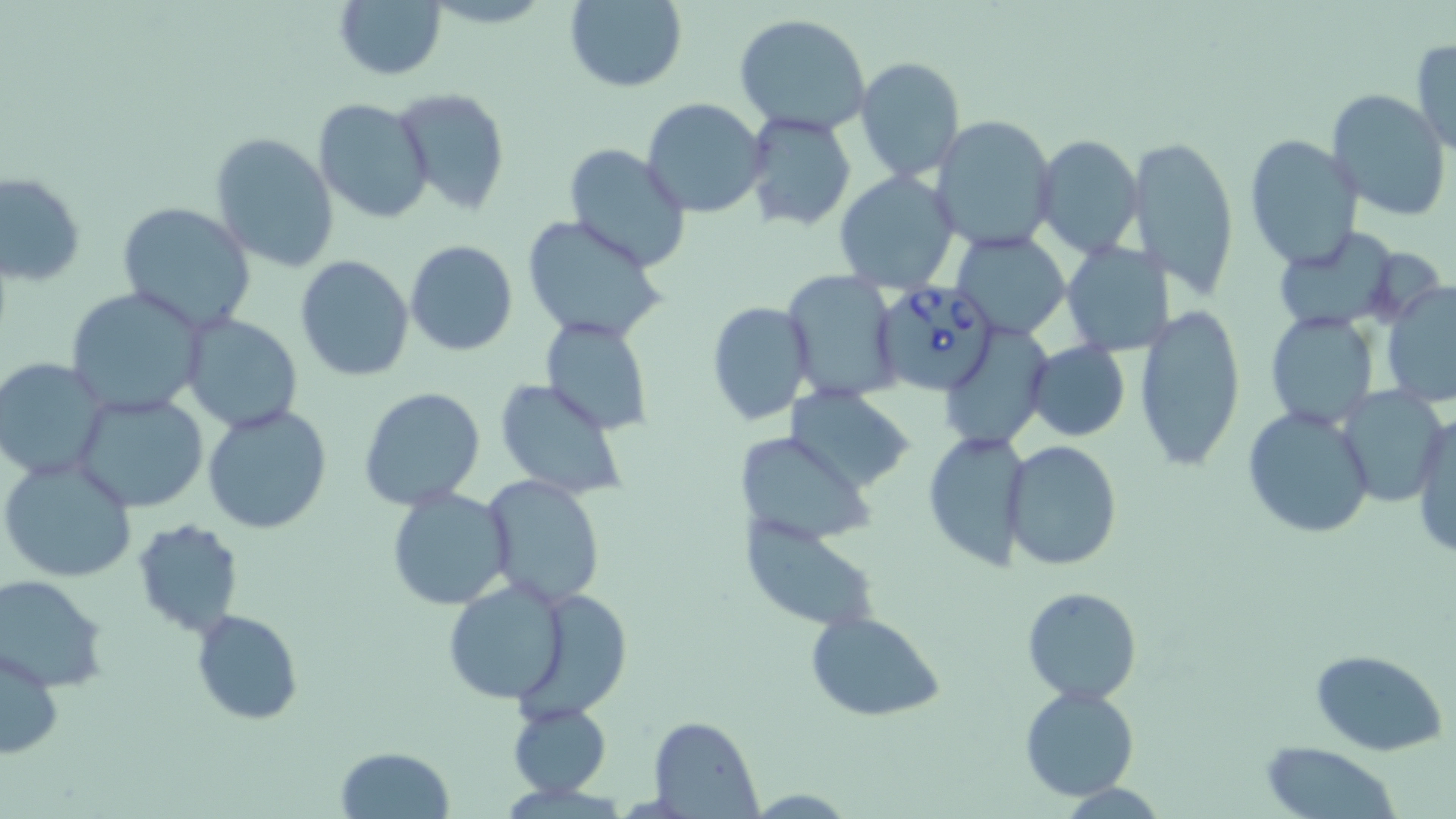
slide-level diagnosis = Babesia divergens
uninfected red blood cell locations = approximate bounding boxes as [x1, y1, x2, y2] in pixels: [563, 0, 688, 92], [333, 2, 447, 80], [733, 14, 875, 137], [1411, 38, 1455, 155], [855, 54, 966, 183], [393, 87, 512, 216], [1327, 89, 1452, 224], [313, 97, 434, 224], [642, 97, 768, 218], [742, 110, 858, 232], [930, 113, 1058, 251], [210, 131, 339, 274], [1033, 135, 1142, 258], [1243, 136, 1363, 270], [1128, 138, 1240, 296], [563, 142, 693, 270], [834, 170, 960, 295], [2, 172, 86, 286], [115, 201, 259, 334], [519, 214, 668, 343], [1271, 229, 1404, 330], [952, 232, 1071, 340], [404, 239, 518, 357], [1061, 239, 1172, 357], [296, 255, 415, 380], [783, 269, 901, 402], [1379, 282, 1456, 411], [66, 287, 205, 416], [706, 301, 815, 426], [1134, 308, 1246, 472], [1265, 311, 1380, 431], [180, 312, 303, 433], [541, 316, 654, 435], [1024, 342, 1130, 442], [2, 357, 112, 482], [495, 378, 629, 502], [358, 386, 486, 510], [1337, 386, 1449, 506], [782, 388, 918, 495], [71, 391, 209, 514], [203, 404, 333, 535], [1243, 406, 1374, 540], [1411, 412, 1456, 561], [921, 429, 1031, 571], [743, 439, 874, 546], [1003, 441, 1122, 572], [1, 456, 133, 584], [480, 475, 605, 608], [386, 487, 514, 610], [131, 519, 244, 637], [740, 519, 879, 629], [0, 575, 112, 692], [444, 581, 570, 704], [1021, 586, 1141, 705], [523, 591, 634, 723], [190, 609, 304, 727], [806, 609, 945, 722], [0, 647, 63, 761], [1310, 648, 1448, 756], [1019, 685, 1140, 801], [507, 701, 611, 799], [647, 715, 761, 816], [1263, 741, 1402, 817], [335, 746, 454, 818]
field of view = one of a larger specimen
magnification = 1000x
image size = 1456×819 pixels
stain = May-Grünwald-Giemsa
preparation = thin blood smear
modality = optical microscopy
Babesia divergens-infected red blood cell locations = approximate bounding boxes as [x1, y1, x2, y2] in pixels: [871, 279, 998, 398]